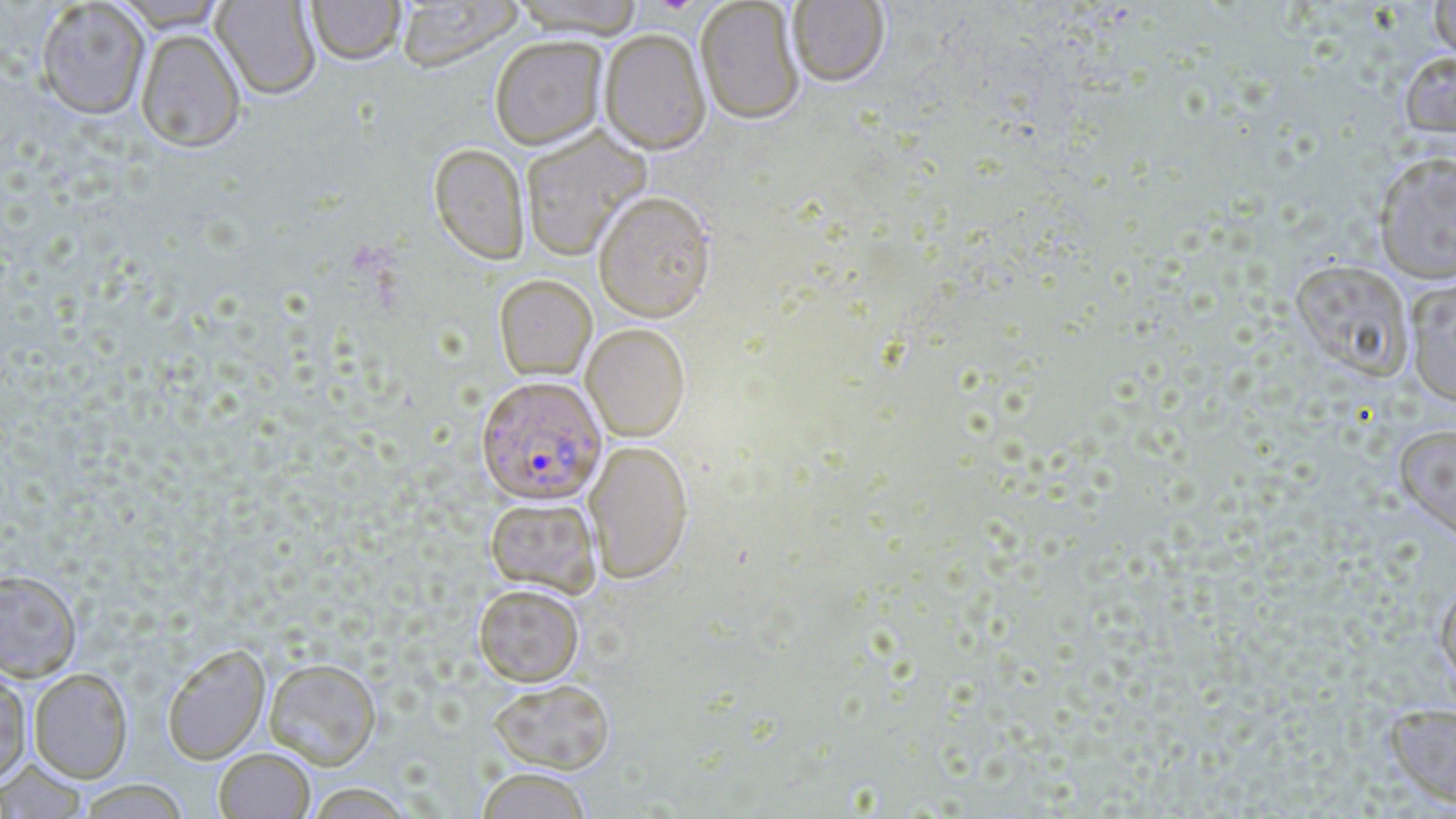
Approximate bounding boxes as (x1,y1)-(x2,y2) corner pairs in pixels. Plasmodium falciparum-infected red blood cell locations: (476,378)-(606,508). Uninfected red blood cell locations: (109,0)-(232,31), (307,0)-(405,67), (395,0)-(524,74), (788,0)-(889,89), (1429,0)-(1456,64), (35,1)-(150,120), (211,1)-(321,101), (507,1)-(645,41), (695,1)-(804,127), (135,29)-(246,153), (599,31)-(711,158), (490,38)-(608,152), (1399,51)-(1456,144), (520,127)-(651,262), (428,145)-(529,267), (1372,151)-(1456,284), (593,195)-(716,326), (1289,258)-(1413,381), (1404,275)-(1456,408), (494,276)-(597,381), (580,325)-(690,443), (1394,424)-(1456,543), (584,441)-(694,586), (485,498)-(601,599), (0,569)-(82,682), (1434,577)-(1456,688), (473,585)-(584,687), (162,645)-(271,765), (263,658)-(382,770), (28,668)-(132,783), (0,670)-(32,784), (488,680)-(615,775), (1383,702)-(1456,810), (214,747)-(315,819), (0,759)-(88,818), (476,768)-(593,819), (75,779)-(190,818), (304,783)-(416,818). Slide-level diagnosis: Plasmodium falciparum. May-Grünwald-Giemsa stain. 1000x magnification. Single field of view. Optical microscopy. Thin blood smear. Image is 1456×819 pixels.